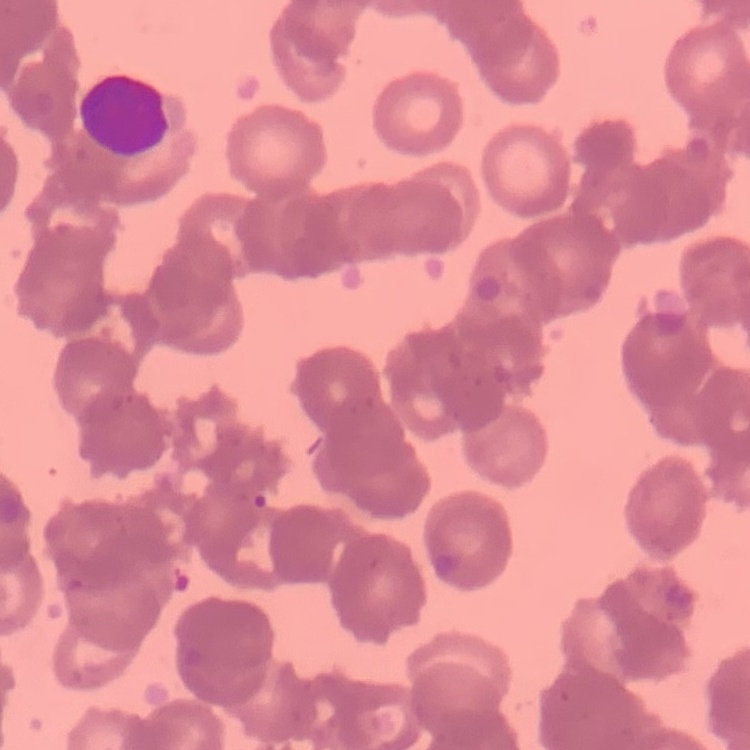
red_blood_cell_morphology: rouleaux formation
image_type: one tile cut from a larger photomicrograph
stain: Field's or Giemsa
preparation: thin blood smear